State the blood parasite species.
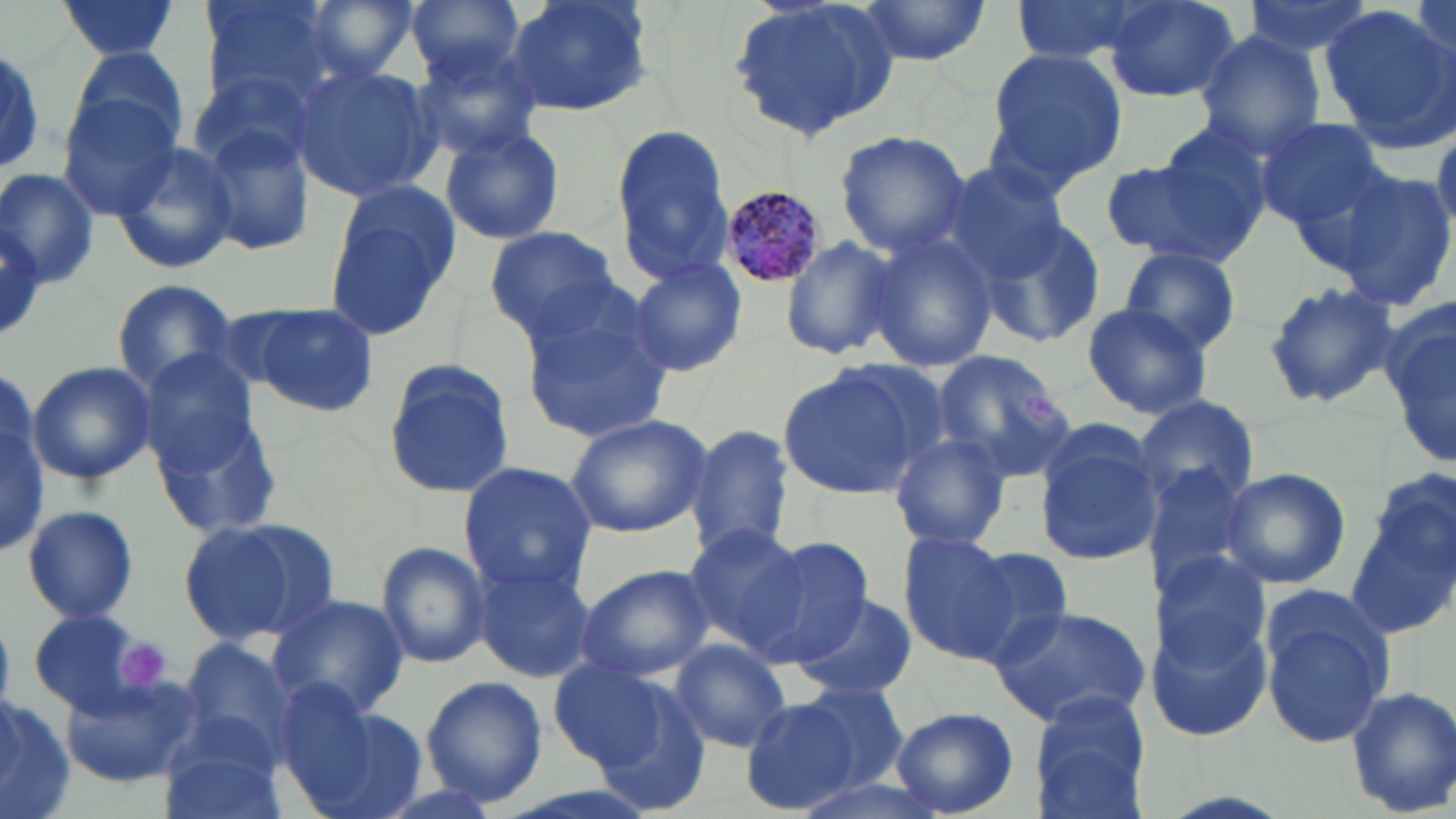

Plasmodium malariae.

platelet_locations: 'approximate bounding boxes as (x1, y1, x2, y2) in pixels: (1018, 386, 1061, 427), (117, 639, 168, 694)'
magnification: 1000x
modality: light microscopy
image_size: 1456×819 pixels
plasmodium_malariae_infected_red_blood_cell_locations: 'approximate bounding boxes as (x1, y1, x2, y2) in pixels: (716, 186, 829, 288)'
preparation: thin blood film
uninfected_red_blood_cell_locations: 'approximate bounding boxes as (x1, y1, x2, y2) in pixels: (199, 0, 338, 107), (295, 0, 424, 85), (406, 0, 525, 85), (503, 0, 655, 120), (727, 0, 903, 140), (857, 0, 988, 66), (1008, 0, 1160, 63), (1102, 0, 1242, 103), (1240, 0, 1381, 63), (54, 1, 183, 58), (1320, 8, 1456, 150), (1194, 30, 1325, 158), (408, 38, 548, 160), (0, 43, 49, 175), (70, 43, 192, 157), (982, 46, 1131, 195), (289, 64, 440, 203), (59, 95, 183, 220), (1255, 117, 1387, 233), (194, 120, 317, 261), (610, 125, 734, 286), (440, 126, 566, 244), (835, 130, 970, 256), (110, 138, 238, 275), (1103, 140, 1269, 272), (938, 161, 1073, 287), (1324, 167, 1454, 311), (0, 169, 100, 288), (323, 183, 464, 338), (973, 211, 1108, 350), (0, 213, 49, 342), (485, 225, 622, 340), (868, 227, 1000, 376), (779, 234, 900, 361), (1117, 246, 1242, 356), (624, 258, 746, 378), (111, 278, 243, 394), (1262, 282, 1400, 408), (518, 289, 676, 443), (1383, 297, 1456, 471), (1081, 302, 1215, 420), (239, 303, 380, 418), (134, 346, 263, 474), (928, 349, 1075, 484), (381, 358, 514, 500), (27, 360, 155, 486), (777, 365, 928, 500), (0, 384, 48, 559), (1130, 394, 1261, 512), (152, 405, 287, 539), (563, 413, 713, 538), (1031, 423, 1164, 567), (685, 425, 797, 563), (888, 433, 1013, 552), (458, 463, 597, 597), (1139, 463, 1262, 598), (1217, 466, 1351, 591), (1346, 483, 1455, 641), (21, 504, 140, 624), (179, 516, 337, 646), (684, 524, 810, 655), (899, 532, 1023, 663), (744, 535, 875, 668), (943, 539, 1077, 663), (374, 540, 491, 670), (1147, 548, 1273, 671), (471, 552, 599, 683), (576, 564, 716, 679), (266, 591, 410, 721), (794, 593, 917, 701), (1258, 597, 1393, 751), (987, 603, 1153, 729), (1148, 608, 1271, 741), (27, 610, 163, 718), (179, 636, 299, 765), (668, 640, 793, 754), (547, 658, 676, 773), (58, 672, 203, 785), (586, 672, 713, 812), (422, 677, 547, 805), (793, 682, 911, 792), (1345, 684, 1456, 818), (1025, 690, 1156, 817), (0, 694, 76, 819), (739, 697, 857, 815), (295, 702, 429, 819), (891, 706, 1017, 818), (155, 719, 290, 819), (786, 774, 949, 818)'
field_of_view: single
stain: May-Grünwald-Giemsa